Identify the parasite.
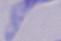
A trypanosome.

Summary:
  - Modality: photomicrograph
  - Magnification: 1000x